Identify the parasite.
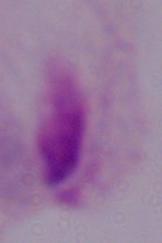
A trichomonad.

magnification = 1000x
modality = micrograph